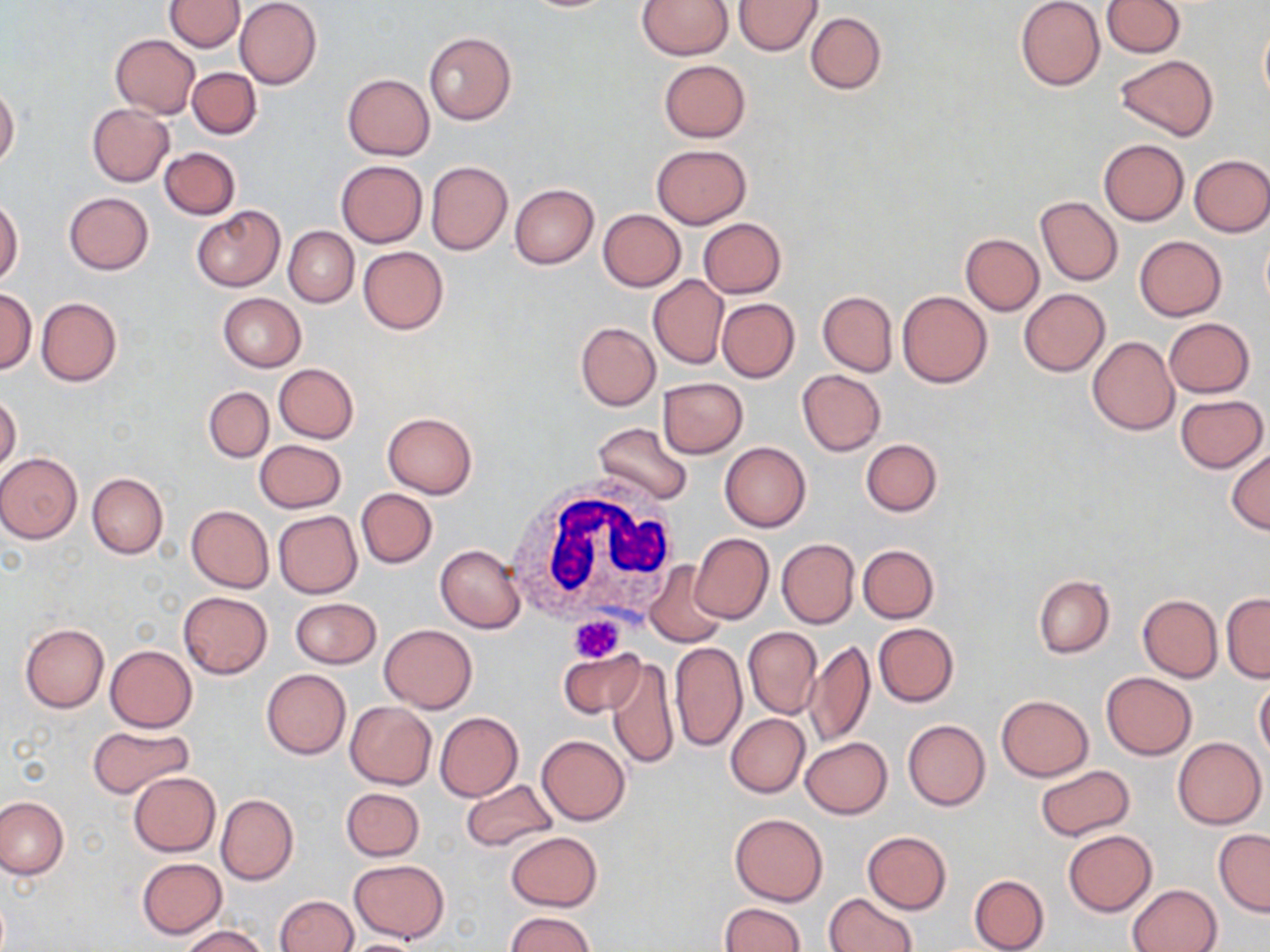

slide-level diagnosis = no evidence of blood parasites
modality = light microscopy
image size = 1270×952 pixels
platelet locations = approximate bounding boxes as [x1, y1, x2, y2] in pixels: [569, 615, 625, 662]
magnification = 1000x
white blood cell locations = approximate bounding boxes as [x1, y1, x2, y2] in pixels: [503, 477, 683, 636]
uninfected red blood cell locations = approximate bounding boxes as [x1, y1, x2, y2] in pixels: [165, 0, 243, 53], [234, 0, 321, 90], [638, 0, 734, 59], [1101, 0, 1185, 58], [733, 1, 823, 56], [1015, 1, 1104, 91], [805, 11, 887, 93], [1259, 15, 1270, 111], [423, 31, 517, 125], [110, 34, 200, 118], [1116, 55, 1219, 141], [658, 59, 750, 142], [186, 67, 261, 139], [343, 73, 434, 159], [0, 84, 19, 169], [88, 105, 173, 185], [1098, 139, 1189, 225], [652, 144, 751, 228], [159, 147, 240, 220], [1189, 154, 1270, 236], [337, 160, 427, 246], [425, 161, 513, 255], [510, 183, 598, 268], [64, 192, 153, 275], [1036, 196, 1122, 286], [0, 197, 23, 286], [192, 206, 286, 292], [597, 209, 686, 291], [698, 218, 786, 298], [284, 226, 358, 306], [961, 233, 1044, 315], [1134, 235, 1227, 321], [358, 246, 449, 334], [648, 275, 728, 369], [1019, 288, 1110, 376], [0, 289, 36, 373], [897, 290, 992, 388], [818, 291, 897, 376], [218, 293, 305, 372], [36, 298, 121, 387], [717, 298, 799, 382], [1164, 318, 1255, 397], [575, 321, 660, 410], [1087, 336, 1179, 435], [274, 364, 358, 443], [797, 369, 886, 455], [658, 377, 747, 458], [204, 386, 273, 462], [0, 392, 21, 474], [1174, 395, 1267, 473], [383, 412, 477, 499], [592, 422, 694, 506], [861, 438, 942, 516], [255, 439, 346, 512], [720, 442, 811, 532], [1228, 447, 1270, 535], [0, 453, 82, 543], [87, 472, 167, 559], [356, 488, 437, 568], [185, 505, 273, 593], [273, 511, 362, 597], [689, 532, 773, 624], [776, 538, 859, 628], [435, 544, 526, 633], [859, 544, 939, 623], [645, 561, 726, 646], [1034, 575, 1115, 657], [179, 592, 272, 678], [1221, 593, 1269, 682], [1138, 594, 1222, 682], [291, 597, 381, 667], [20, 623, 109, 712], [873, 623, 959, 707], [380, 624, 477, 711], [743, 626, 822, 719], [805, 640, 875, 747], [670, 641, 746, 752], [105, 644, 196, 732], [559, 648, 645, 719], [606, 657, 680, 768], [262, 669, 351, 759], [1101, 673, 1197, 760], [1254, 678, 1270, 761], [996, 694, 1094, 781], [345, 700, 435, 789], [435, 712, 523, 801], [725, 713, 809, 798], [902, 719, 991, 811], [86, 726, 193, 798], [536, 735, 630, 825], [800, 737, 891, 818], [1172, 737, 1266, 829], [1034, 764, 1135, 841], [128, 771, 220, 857], [461, 779, 557, 851], [341, 788, 424, 860], [216, 793, 298, 884], [0, 796, 68, 879], [730, 813, 827, 905], [1214, 828, 1270, 915], [1063, 829, 1156, 915], [506, 831, 602, 911], [863, 831, 951, 914], [136, 857, 228, 938], [349, 860, 449, 944], [969, 875, 1050, 952], [1128, 883, 1222, 952], [826, 891, 917, 952], [274, 895, 358, 952], [718, 903, 806, 952], [504, 912, 596, 952], [180, 925, 269, 952], [337, 938, 427, 952]
preparation = thin blood smear
stain = May-Grünwald-Giemsa
field of view = one of a larger specimen